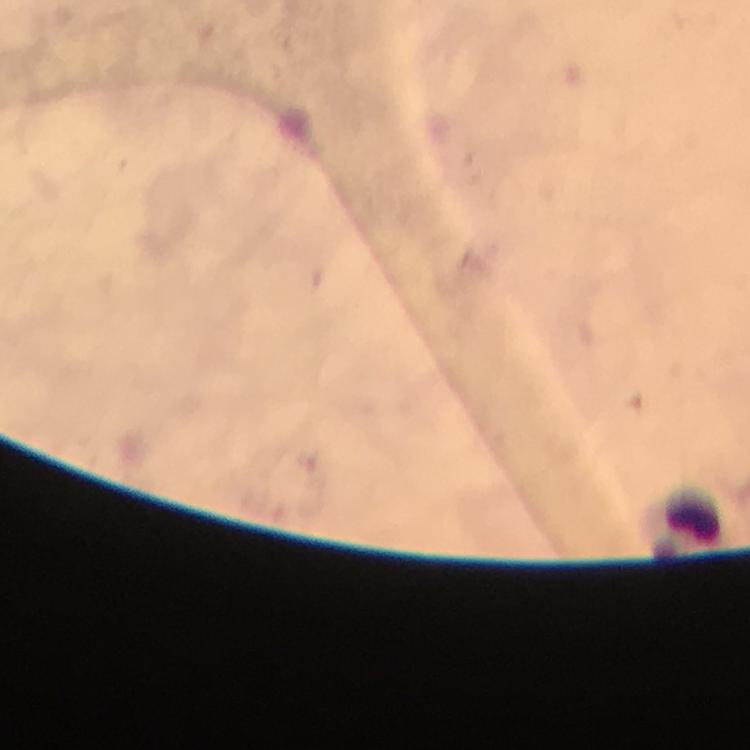
Approximate centers as (x, y) in pixels.
Summary:
  - Leukocyte locations: (685, 524)
  - Magnification: 100x
  - Image size: 750×750 pixels
  - Context: from a malaria diagnostic workup
  - Plasmodium parasites: none seen
  - Immersion oil: applied
  - Stain: Giemsa
  - Preparation: thick blood smear
  - Cropped from: one field of view
  - Capture: smartphone camera through the microscope